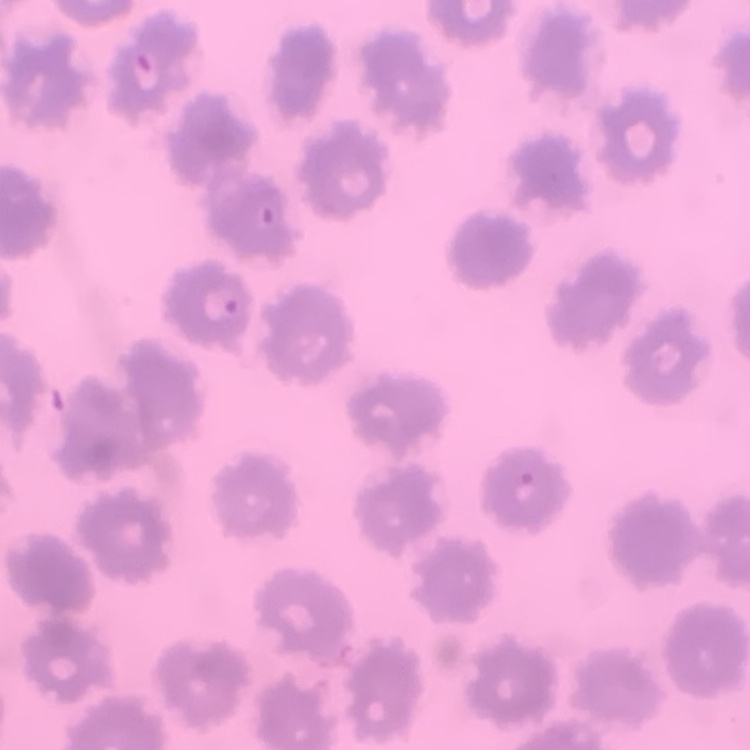
Summary:
  - Red blood cell morphology: no rouleaux formation
  - Image type: square crop of a larger photomicrograph
  - Stain: Field's or Giemsa
  - Preparation: thin blood film